Outline each Plasmodium ovale-infected red blood cell.
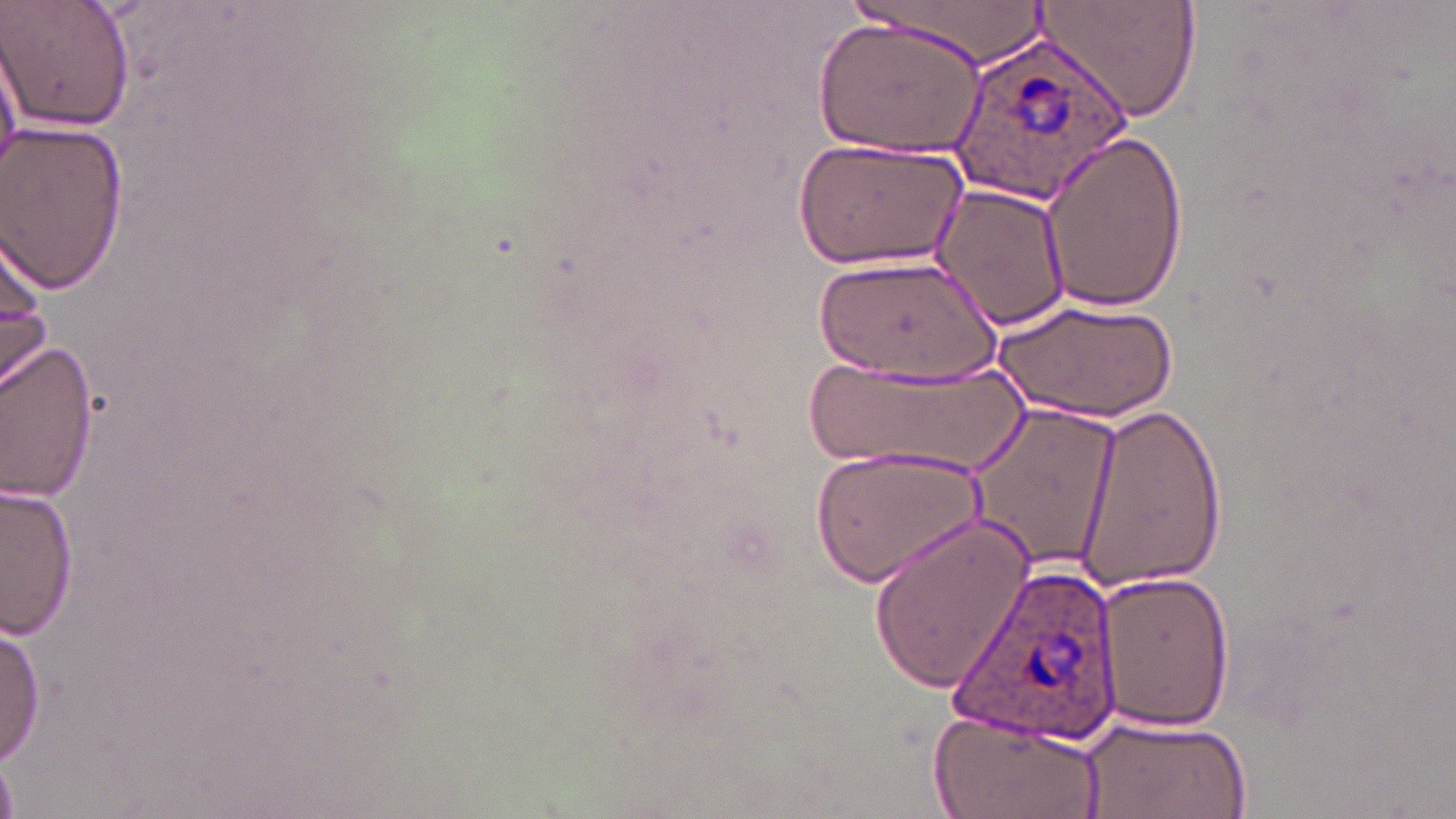

Approximate bounding boxes as (x1, y1, x2, y2) in pixels.
Plasmodium ovale-infected red blood cells: (951, 30, 1138, 207), (955, 564, 1122, 749).

slide-level diagnosis = Plasmodium ovale
modality = light microscopy
magnification = 1000x
field of view = single
preparation = thin blood film
uninfected red blood cell locations = approximate bounding boxes as (x1, y1, x2, y2) in pixels: (1, 0, 135, 135), (839, 0, 1057, 66), (1034, 0, 1202, 122), (813, 18, 988, 159), (0, 32, 22, 184), (0, 121, 130, 296), (1038, 129, 1191, 313), (790, 138, 967, 271), (926, 182, 1072, 333), (0, 227, 54, 400), (807, 256, 1004, 384), (998, 297, 1181, 422), (0, 335, 101, 505), (800, 353, 1034, 479), (1072, 399, 1227, 592), (970, 404, 1125, 576), (812, 439, 992, 589), (2, 479, 82, 643), (866, 514, 1038, 696), (1096, 570, 1235, 734), (0, 616, 47, 768), (927, 705, 1110, 819), (1080, 714, 1253, 817)
stain = May-Grünwald-Giemsa
image size = 1456×819 pixels